Assess the morphology of the erythrocytes.
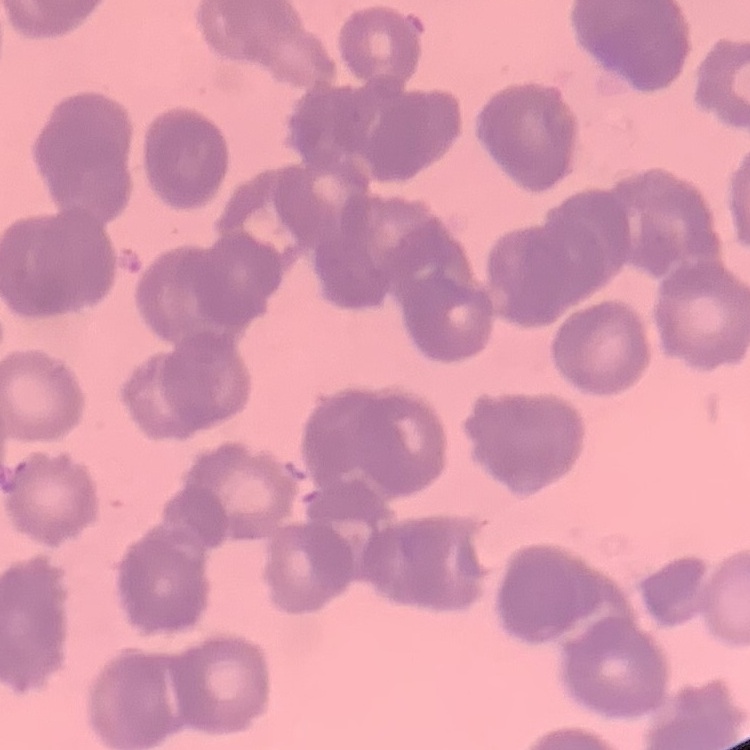

Rouleaux formation.

image type = one tile cut from a larger photomicrograph
preparation = thin blood film
stain = Field's or Giemsa